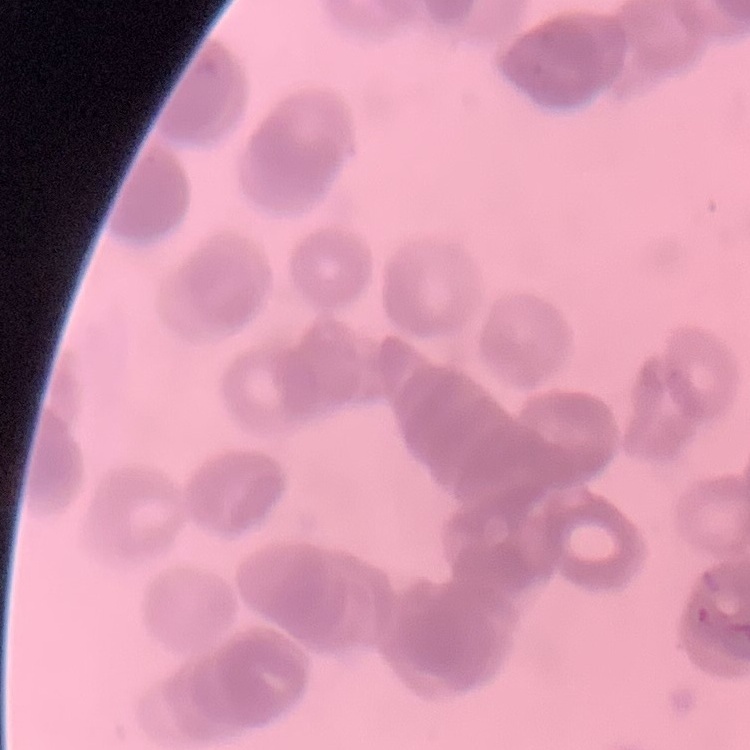
The red blood cells exhibit rouleaux formation. Thin peripheral smear. Field's or Giemsa stain. Square crop of a larger photomicrograph.